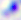

magnification = 400x
modality = micrograph
identification = Toxoplasma gondii